State which parasite is depicted.
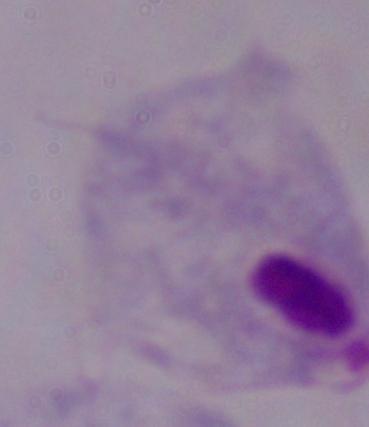
A trichomonad.

magnification: 1000x
modality: photomicrograph